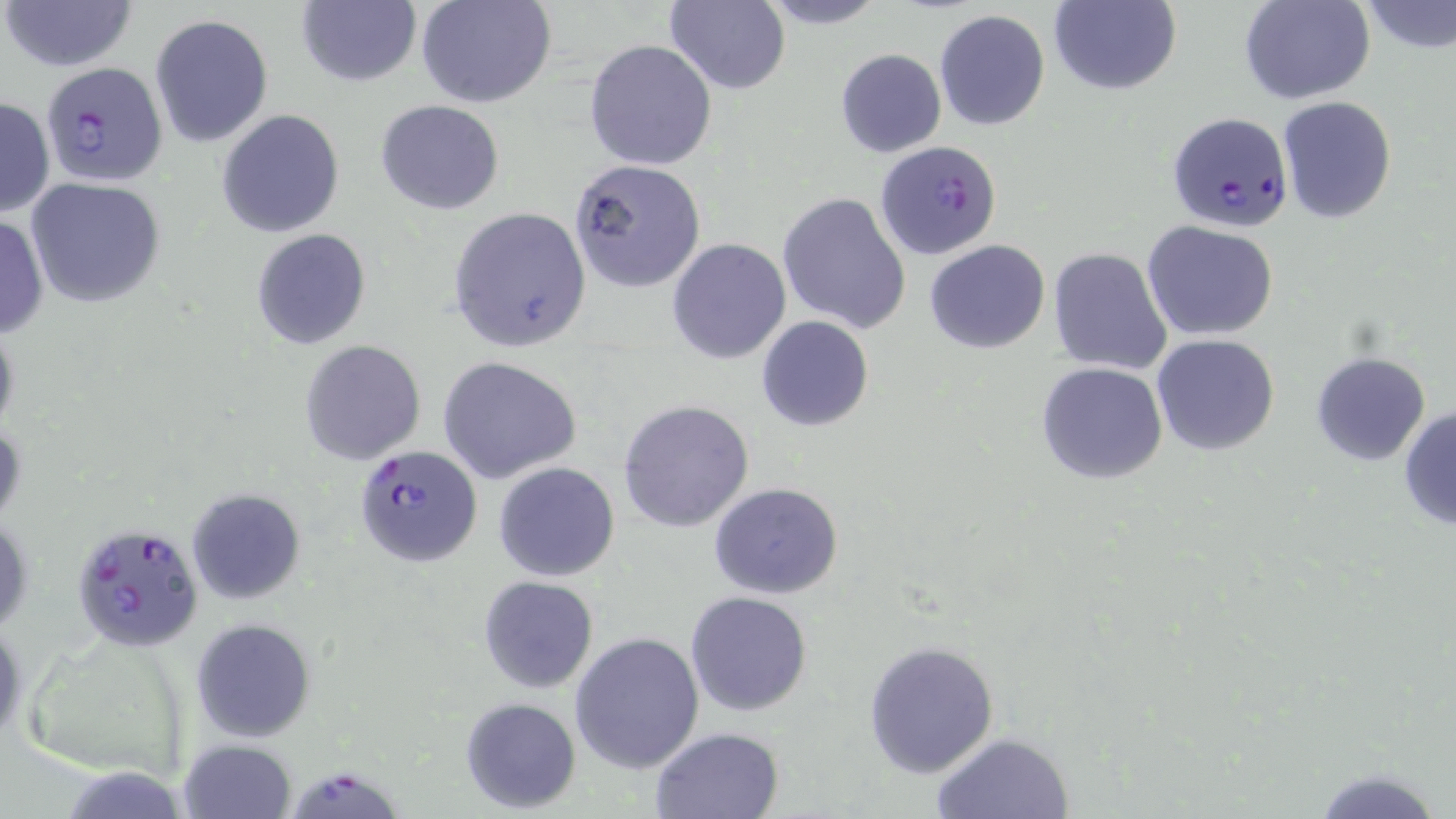
Summary:
  - Coordinate format: approximate bounding boxes as [x1, y1, x2, y2] in pixels
  - Uninfected red blood cell locations: [2, 0, 137, 72], [296, 0, 421, 88], [417, 0, 556, 108], [664, 0, 789, 95], [752, 0, 892, 29], [1047, 0, 1182, 96], [1239, 0, 1375, 105], [1358, 1, 1456, 54], [934, 9, 1051, 131], [150, 14, 273, 148], [584, 38, 717, 172], [835, 48, 946, 157], [1276, 96, 1397, 223], [0, 97, 54, 219], [376, 99, 505, 214], [216, 109, 346, 237], [569, 159, 707, 292], [25, 178, 166, 307], [777, 192, 912, 333], [448, 206, 591, 351], [0, 215, 48, 338], [1141, 221, 1279, 340], [250, 228, 373, 351], [667, 238, 792, 363], [924, 238, 1051, 354], [1048, 247, 1173, 376], [0, 315, 20, 445], [756, 315, 873, 430], [1151, 334, 1281, 456], [299, 339, 424, 465], [1310, 352, 1431, 465], [437, 356, 585, 485], [1035, 363, 1169, 484], [618, 400, 754, 532], [1397, 406, 1456, 531], [493, 461, 620, 582], [708, 482, 845, 600], [185, 487, 305, 604], [1, 511, 33, 637], [478, 576, 598, 693], [686, 590, 814, 716], [0, 616, 25, 750], [189, 619, 315, 742], [570, 631, 704, 774], [864, 640, 1001, 777], [460, 697, 581, 811], [649, 726, 783, 818], [931, 732, 1073, 817], [177, 739, 297, 819], [1308, 765, 1443, 819]
  - Plasmodium falciparum-infected red blood cell locations: [42, 64, 169, 187], [1165, 111, 1293, 234], [876, 141, 999, 262], [355, 444, 483, 568], [76, 525, 198, 649], [282, 763, 405, 819]
  - Slide-level diagnosis: Plasmodium falciparum
  - Stain: May-Grünwald-Giemsa
  - Preparation: thin blood film
  - Modality: light microscopy
  - Field of view: single
  - Magnification: 1000x
  - Image size: 1456×819 pixels